Describe the morphology of the erythrocytes.
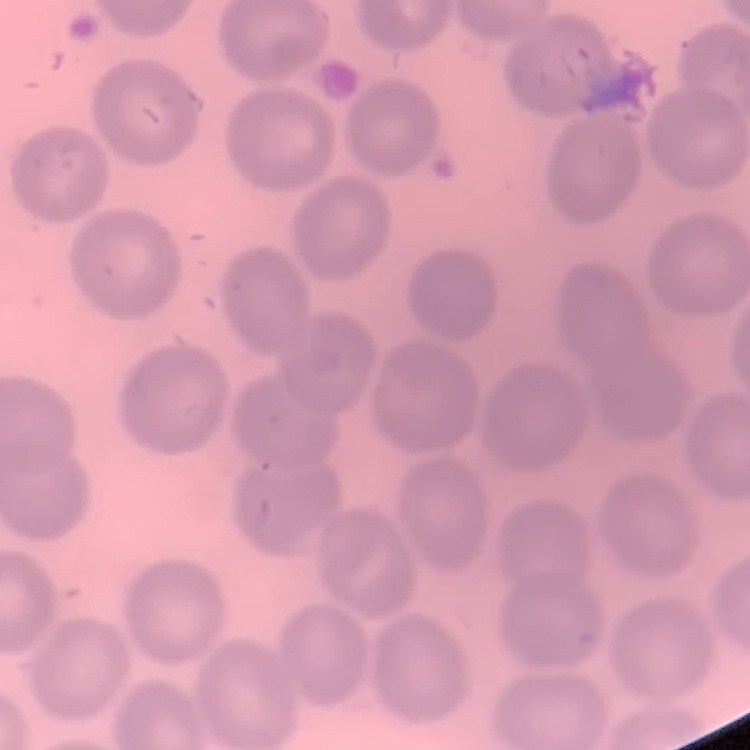

No rouleaux formation.

Thin blood film. Square crop of a larger photomicrograph. Field's or Giemsa stain.